Point out each leukocyte.
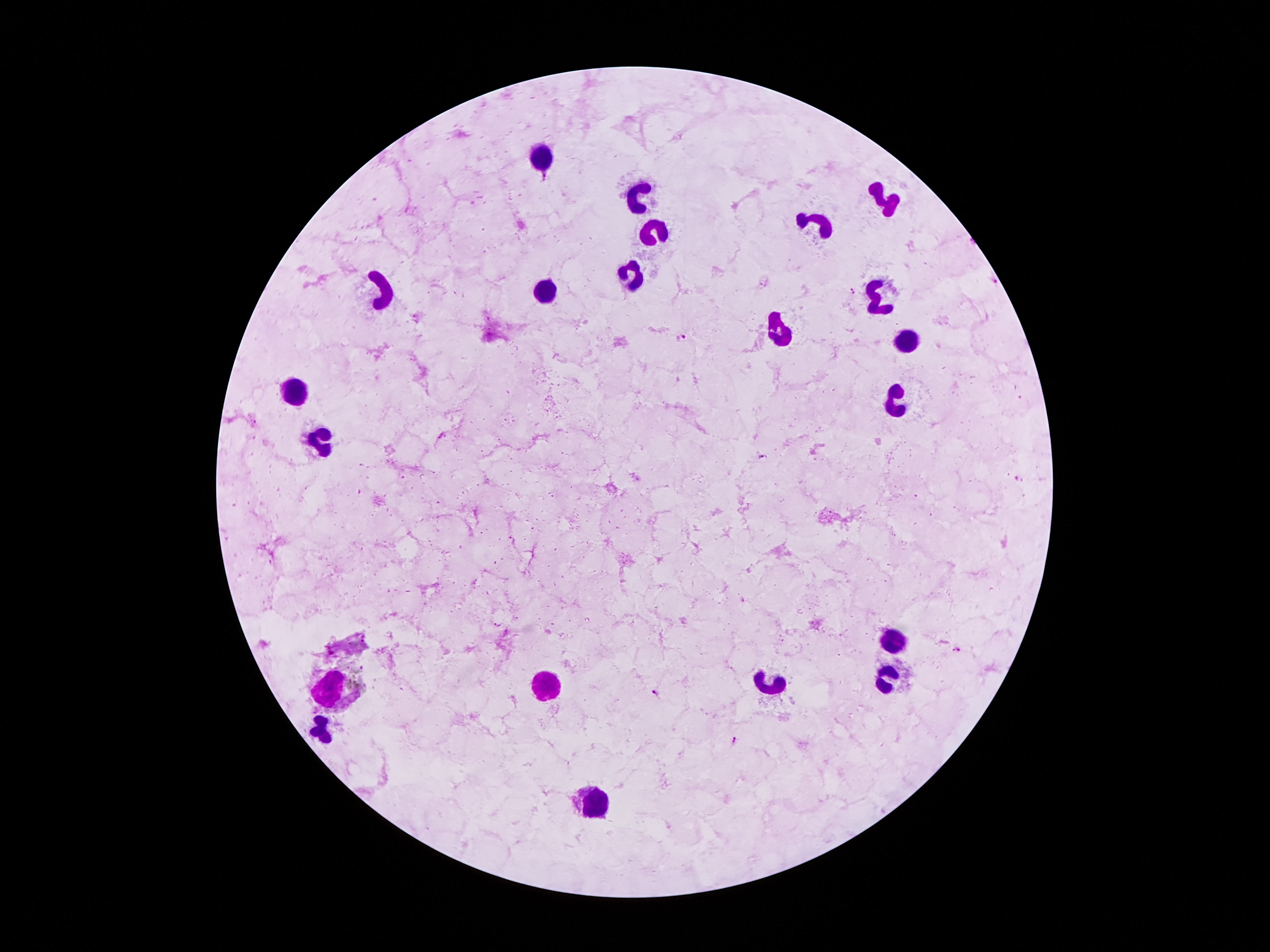
Approximate centers as {x, y} in pixels.
Leukocytes: {542, 158}, {638, 193}, {888, 205}, {815, 224}, {652, 232}, {628, 274}, {542, 289}, {381, 290}, {882, 298}, {778, 331}, {904, 342}, {297, 392}, {894, 406}, {319, 440}, {895, 644}, {886, 678}, {770, 682}, {549, 686}, {339, 687}, {324, 729}, {594, 802}.

Summary:
  - Plasmodium parasite locations: {995, 280}, {852, 290}, {682, 337}, {762, 456}, {1017, 476}, {956, 648}, {657, 693}, {735, 740}
  - Image size: 1270×952 pixels
  - Capture: smartphone through the microscope eyepiece
  - Preparation: thick blood smear
  - Patient malaria status: infected with Plasmodium falciparum
  - Magnification: 100x
  - Stain: Giemsa
  - Field of view: one from this slide